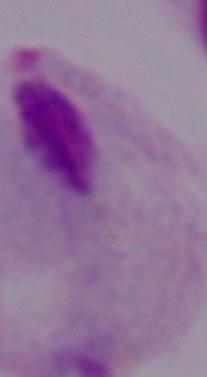
Summary:
  - Magnification: 1000x
  - Modality: micrograph
  - Identification: trichomonad